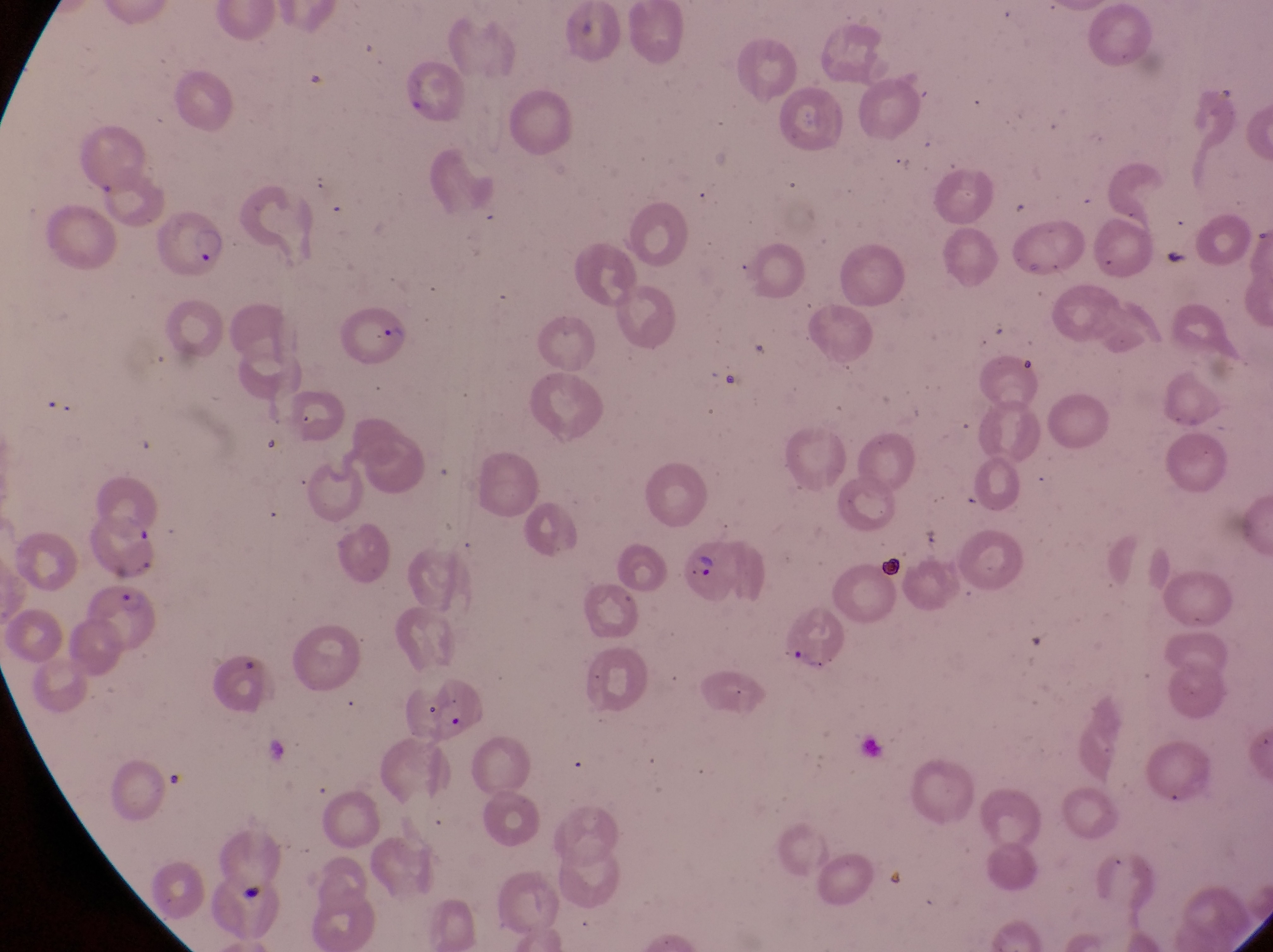

Approximate bounding boxes as {left, top, right, bottom} in pixels.
Summary:
  - Parasitised red blood cell locations: {152, 209, 226, 284}, {340, 309, 409, 367}, {681, 535, 756, 610}, {80, 580, 167, 663}, {784, 609, 858, 679}, {430, 679, 488, 741}
  - Capture: smartphone photograph through the eyepiece of an Olympus CX-23 microscope
  - Magnification: 1000x
  - Field of view: single
  - Image size: 1273×952 pixels
  - Preparation: thin blood smear
  - Country: Uganda